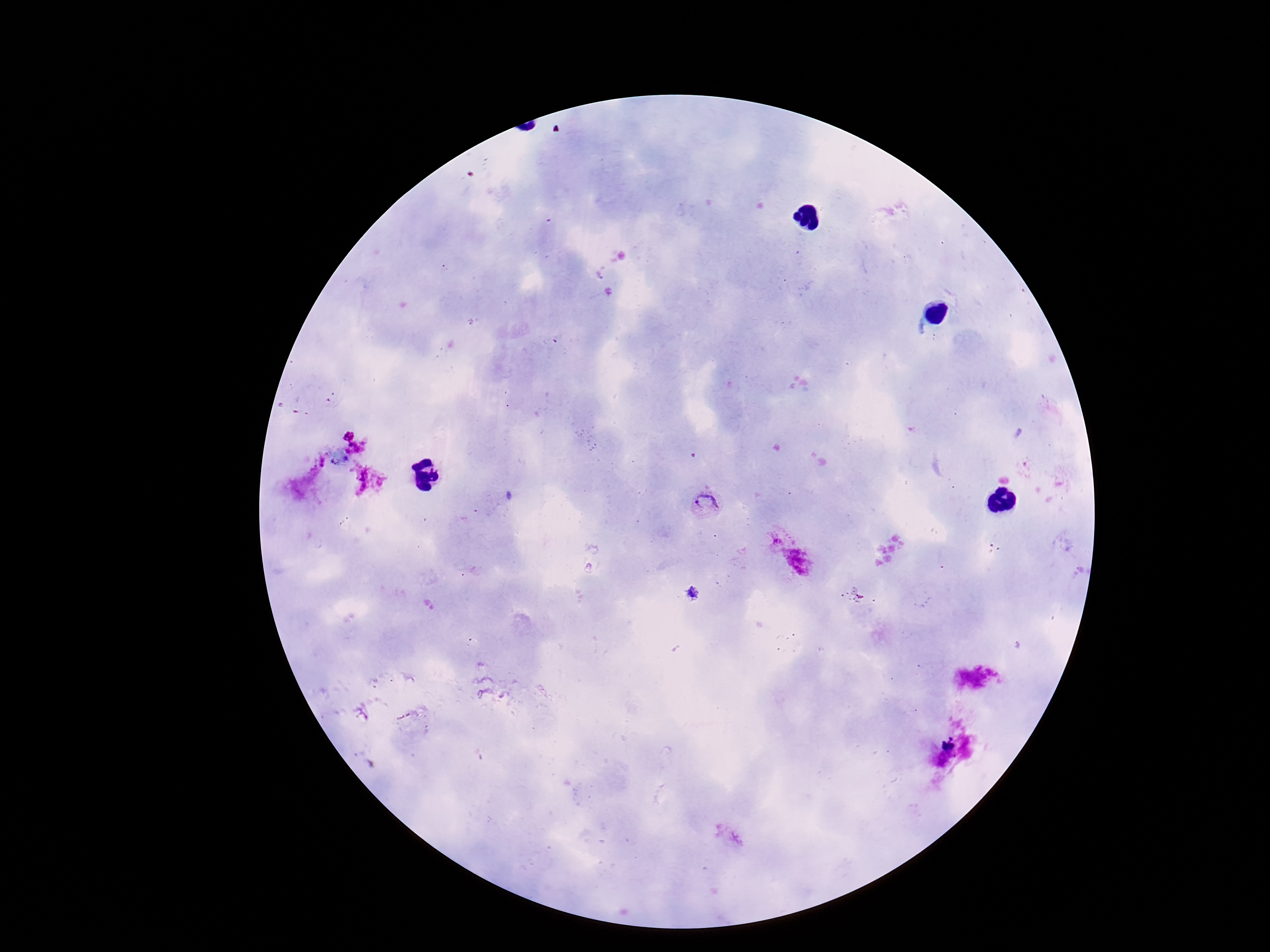 Approximate centers as {x, y} in pixels. Plasmodium parasite locations: {707, 502}, {776, 540}, {798, 563}. Giemsa stain. Smartphone photograph taken through the microscope eyepiece. Patient malaria status: positive. One field from this slide. Image is 1270×952 pixels. Thick blood film. 100x magnification.